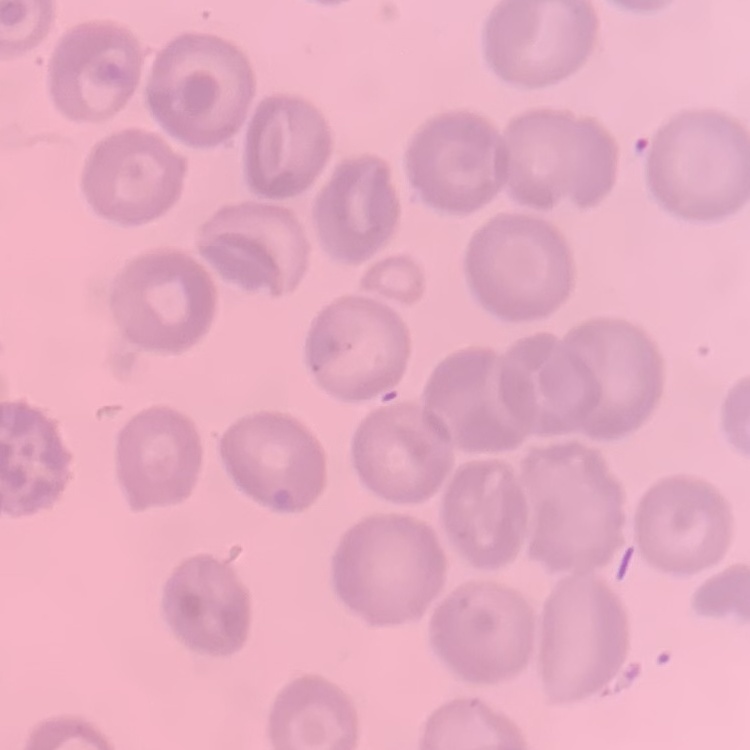
red blood cell morphology = no rouleaux formation
preparation = thin blood film
image type = square crop of a larger photomicrograph
stain = Field's or Giemsa